State the preparation type.
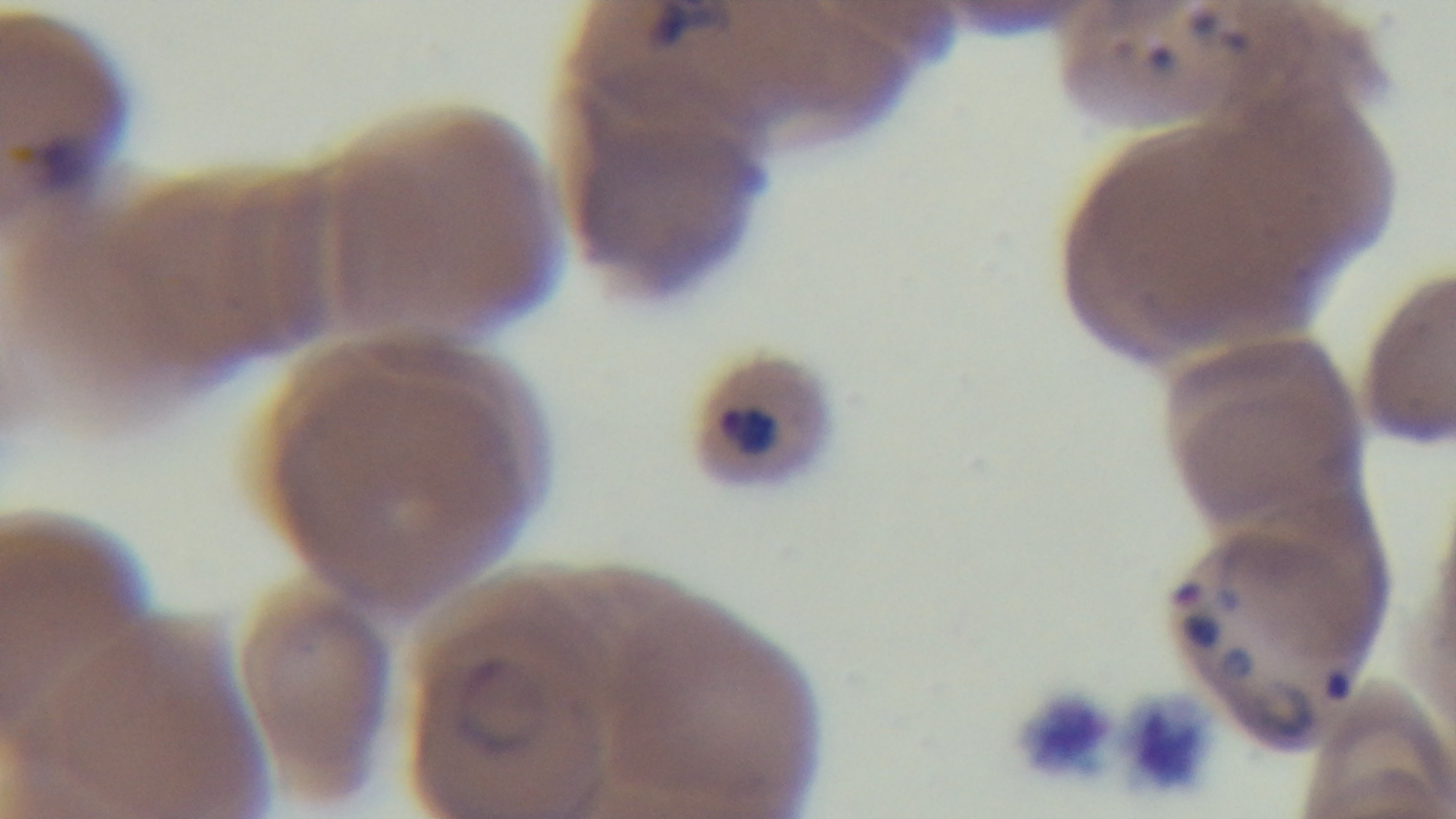
A thin smear.

Summary:
  - Stain: Giemsa
  - Field of view: single
  - Objective: 100x oil immersion
  - Malaria status: positive
  - Modality: light microscopy
  - Capture: mounted 4K digital camera